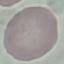

result: negative for malaria parasites
image_type: cell patch, automatically extracted from a larger field of view and resized to 64 × 64 pixels
capture: smartphone camera at the microscope eyepiece
stain: Giemsa
preparation: thin blood smear